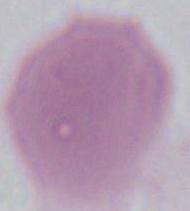
Summary:
  - Modality: micrograph
  - Identification: red blood cell
  - Magnification: 1000x